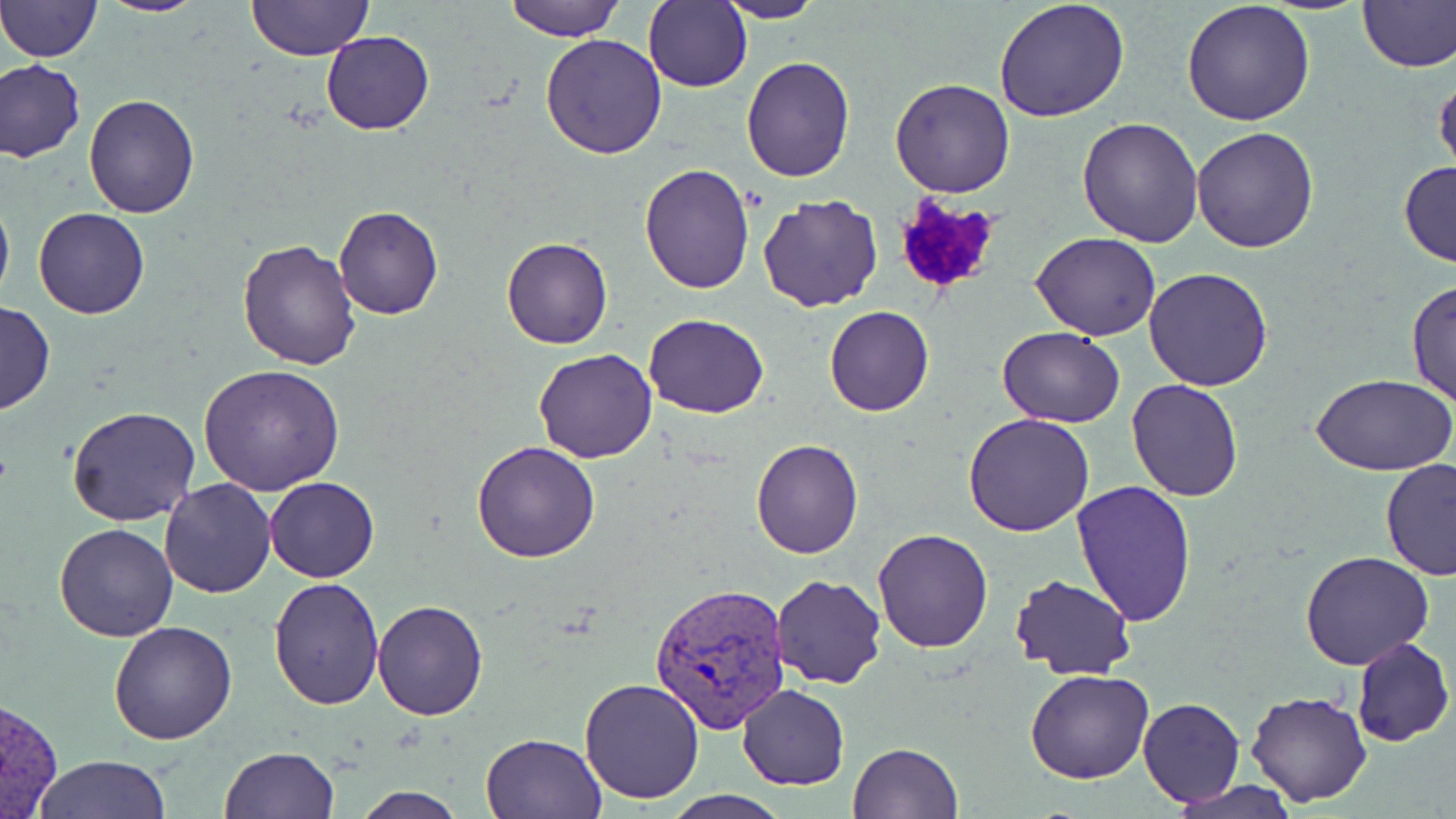
Approximate bounding boxes as (x1, y1, x2, y2) in pixels. Plasmodium vivax-infected red blood cell locations: (647, 581, 791, 732). Platelet locations: (891, 193, 1004, 300). Uninfected red blood cell locations: (0, 0, 103, 62), (96, 0, 208, 17), (247, 0, 370, 60), (506, 0, 622, 41), (645, 0, 752, 94), (715, 0, 825, 24), (995, 0, 1131, 121), (1182, 0, 1315, 126), (1356, 0, 1456, 71), (321, 31, 434, 135), (540, 33, 668, 159), (739, 56, 855, 180), (1, 60, 86, 162), (890, 78, 1016, 198), (82, 94, 200, 218), (1076, 116, 1204, 248), (1191, 128, 1318, 252), (1398, 160, 1456, 268), (639, 164, 754, 293), (636, 172, 875, 299), (0, 188, 13, 308), (758, 194, 885, 313), (334, 206, 443, 320), (32, 207, 150, 319), (1031, 233, 1161, 341), (502, 237, 612, 349), (238, 240, 361, 371), (1143, 267, 1276, 392), (1407, 281, 1455, 410), (0, 302, 56, 414), (824, 307, 933, 415), (645, 313, 767, 419), (999, 328, 1126, 429), (532, 347, 657, 463), (198, 364, 345, 495), (1312, 372, 1456, 476), (1126, 377, 1247, 500), (65, 406, 201, 526), (963, 413, 1095, 537), (751, 438, 862, 558), (472, 441, 601, 562), (1381, 459, 1455, 581), (266, 476, 379, 582), (159, 478, 276, 598), (1072, 478, 1198, 625), (54, 523, 178, 641), (871, 529, 993, 653), (1299, 550, 1436, 671), (267, 574, 383, 710), (1010, 574, 1137, 679), (771, 575, 886, 689), (371, 598, 488, 720), (108, 620, 238, 744), (1349, 637, 1455, 747), (1024, 669, 1154, 785), (578, 678, 704, 804), (736, 684, 849, 789), (1245, 691, 1374, 808), (1136, 696, 1246, 806), (479, 731, 605, 818), (847, 743, 963, 819), (218, 747, 340, 818), (32, 755, 175, 819), (1166, 780, 1302, 817), (350, 788, 468, 819), (662, 790, 793, 819). Slide-level diagnosis: Plasmodium vivax. Thin blood smear. Optical microscopy. Single field of view. Image is 1456×819 pixels. May-Grünwald-Giemsa-stained preparation. 1000x magnification.